Report the malaria status of this cell.
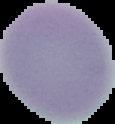

Uninfected.

Segmented cell region on a black background. From a thin blood film. Image is 115×124 pixels.